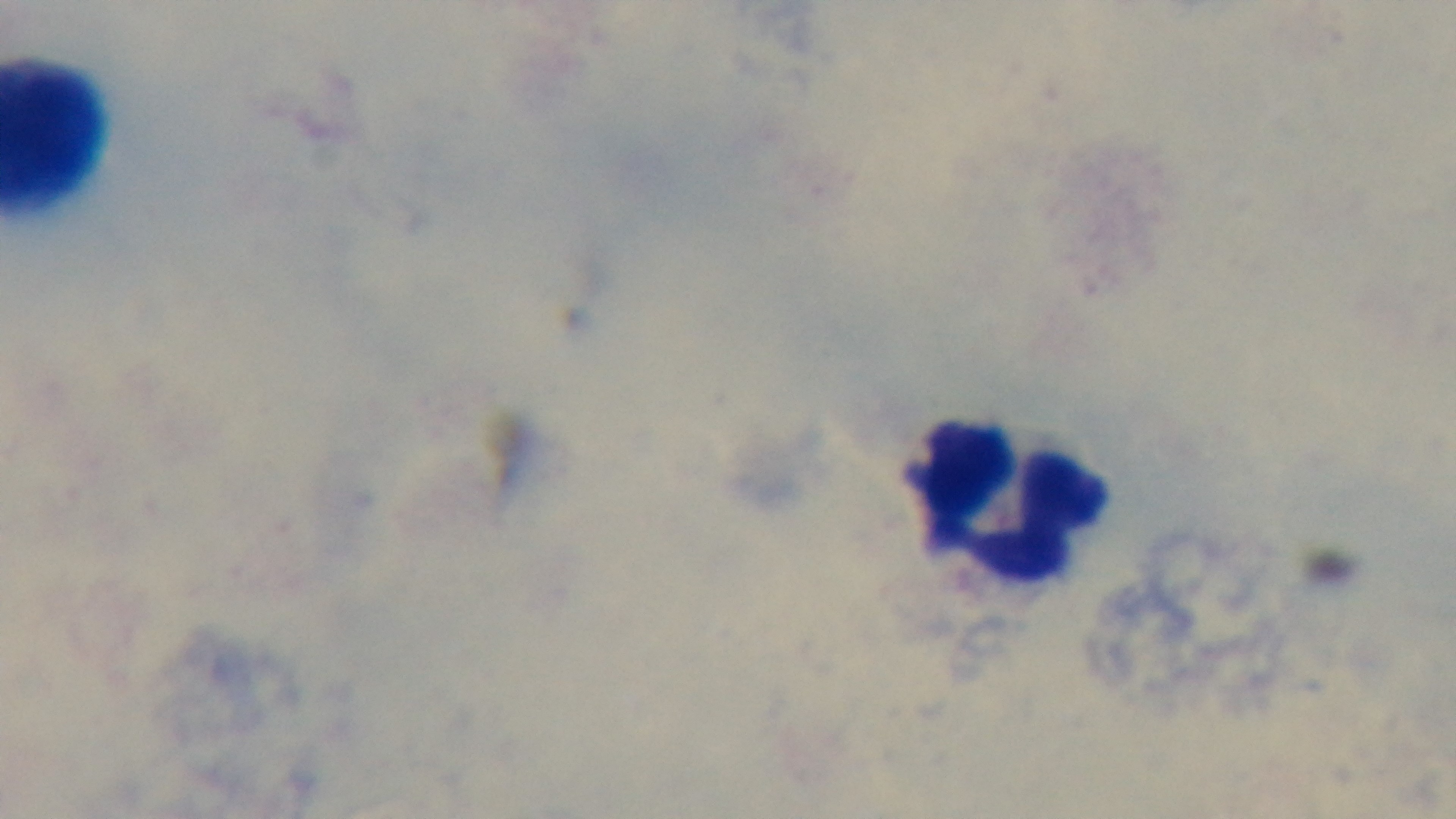

stain = Giemsa
malaria status = uninfected
objective = 100x oil immersion
modality = light microscopy
capture = mounted 4K digital camera
preparation = thick smear
field of view = one from the slide